State which cell type is depicted.
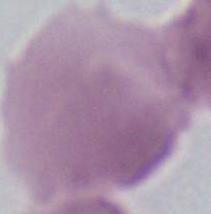

An erythrocyte.

1000x magnification. Photomicrograph.